Outline each Plasmodium malariae-infected red blood cell.
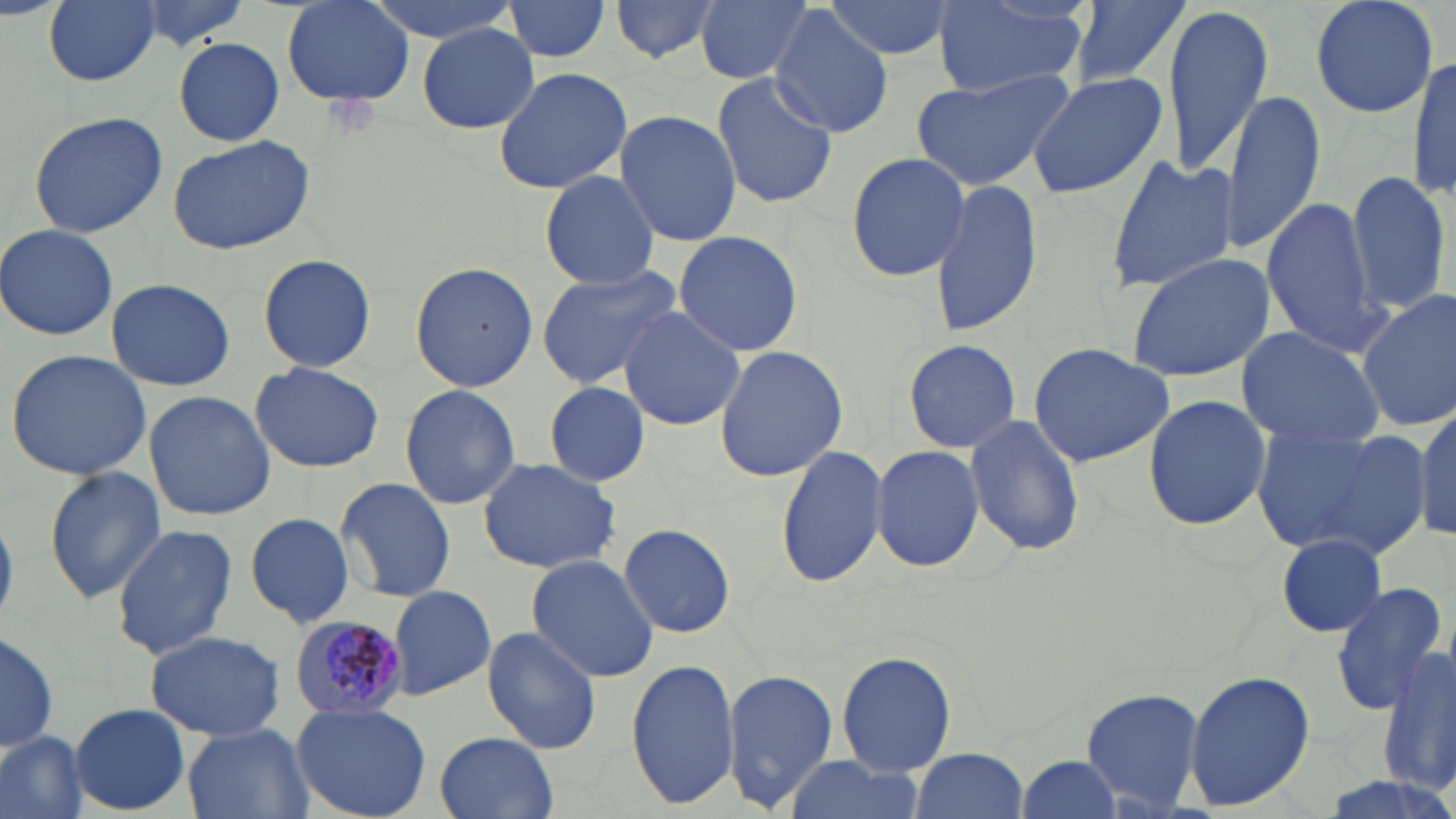
Approximate bounding boxes as named x1/y1/x2/y2 corners in pixels.
Plasmodium malariae-infected red blood cells: (x1=290, y1=614, x2=414, y2=721).

Uninfected red blood cell locations: (x1=43, y1=0, x2=162, y2=87), (x1=128, y1=0, x2=257, y2=49), (x1=279, y1=0, x2=417, y2=110), (x1=368, y1=0, x2=519, y2=43), (x1=503, y1=0, x2=613, y2=65), (x1=608, y1=0, x2=728, y2=63), (x1=696, y1=0, x2=815, y2=85), (x1=823, y1=0, x2=955, y2=60), (x1=1067, y1=0, x2=1195, y2=94), (x1=1308, y1=0, x2=1442, y2=119), (x1=935, y1=1, x2=1086, y2=99), (x1=1162, y1=3, x2=1274, y2=177), (x1=770, y1=8, x2=892, y2=136), (x1=418, y1=22, x2=541, y2=133), (x1=172, y1=36, x2=286, y2=147), (x1=1409, y1=48, x2=1456, y2=208), (x1=492, y1=65, x2=633, y2=194), (x1=911, y1=68, x2=1072, y2=189), (x1=1025, y1=70, x2=1169, y2=198), (x1=710, y1=72, x2=840, y2=210), (x1=1223, y1=90, x2=1326, y2=257), (x1=614, y1=109, x2=742, y2=248), (x1=27, y1=110, x2=169, y2=239), (x1=166, y1=132, x2=318, y2=255), (x1=844, y1=152, x2=971, y2=283), (x1=1103, y1=155, x2=1239, y2=294), (x1=1346, y1=168, x2=1451, y2=319), (x1=539, y1=170, x2=662, y2=289), (x1=928, y1=177, x2=1044, y2=338), (x1=1261, y1=198, x2=1386, y2=356), (x1=1, y1=224, x2=120, y2=341), (x1=672, y1=230, x2=804, y2=356), (x1=1126, y1=251, x2=1276, y2=383), (x1=258, y1=253, x2=376, y2=374), (x1=409, y1=262, x2=538, y2=393), (x1=534, y1=264, x2=685, y2=389), (x1=106, y1=278, x2=236, y2=390), (x1=1355, y1=289, x2=1456, y2=432), (x1=617, y1=306, x2=745, y2=431), (x1=1235, y1=326, x2=1388, y2=450), (x1=903, y1=338, x2=1022, y2=454), (x1=1026, y1=342, x2=1175, y2=466), (x1=713, y1=344, x2=847, y2=482), (x1=6, y1=349, x2=154, y2=481), (x1=250, y1=361, x2=383, y2=473), (x1=543, y1=382, x2=654, y2=484), (x1=399, y1=384, x2=521, y2=510), (x1=144, y1=390, x2=275, y2=521), (x1=1141, y1=392, x2=1273, y2=534), (x1=1412, y1=405, x2=1456, y2=544), (x1=963, y1=413, x2=1086, y2=556), (x1=1252, y1=425, x2=1428, y2=561), (x1=775, y1=443, x2=889, y2=590), (x1=870, y1=445, x2=984, y2=573), (x1=475, y1=458, x2=622, y2=573), (x1=42, y1=465, x2=167, y2=603), (x1=334, y1=476, x2=456, y2=602), (x1=243, y1=511, x2=356, y2=627), (x1=619, y1=522, x2=736, y2=640), (x1=111, y1=524, x2=239, y2=659), (x1=1276, y1=532, x2=1389, y2=636), (x1=525, y1=554, x2=662, y2=683), (x1=1329, y1=581, x2=1449, y2=715), (x1=386, y1=583, x2=497, y2=700), (x1=481, y1=626, x2=602, y2=754), (x1=0, y1=629, x2=59, y2=753), (x1=145, y1=629, x2=285, y2=741), (x1=1380, y1=644, x2=1455, y2=804), (x1=834, y1=648, x2=961, y2=778), (x1=626, y1=659, x2=741, y2=808), (x1=724, y1=669, x2=840, y2=810), (x1=1182, y1=669, x2=1316, y2=811), (x1=1081, y1=687, x2=1206, y2=814), (x1=292, y1=702, x2=433, y2=819), (x1=70, y1=704, x2=191, y2=815), (x1=181, y1=724, x2=313, y2=819), (x1=0, y1=731, x2=86, y2=819), (x1=435, y1=732, x2=559, y2=819), (x1=910, y1=748, x2=1028, y2=819), (x1=786, y1=753, x2=922, y2=819), (x1=1016, y1=754, x2=1127, y2=819). Slide-level diagnosis: Plasmodium malariae. Thin blood smear. 1000x magnification. Light microscopy. Image is 1456×819 pixels. One field of a larger specimen. May-Grünwald-Giemsa-stained preparation.